Locate and identify every blood parasite.
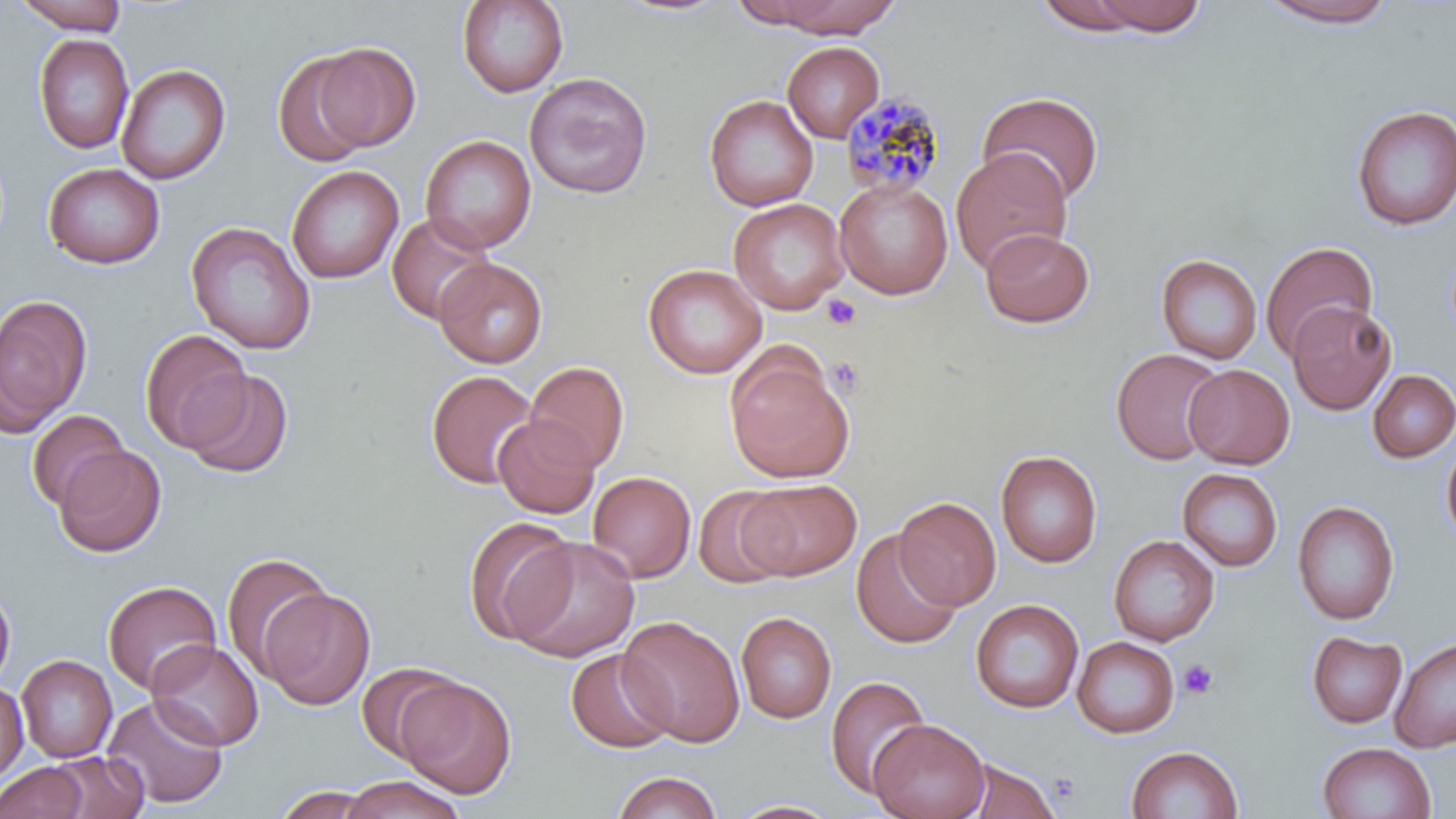
Approximate bounding boxes as named x1/y1/x2/y2 corners in pixels.
Plasmodium malariae-infected red blood cells: (x1=840, y1=90, x2=946, y2=198).
No Plasmodium falciparum, Plasmodium ovale, Plasmodium vivax, Babesia divergens, or Trypanosoma brucei observed.

Summary:
  - Platelet locations: (x1=823, y1=294, x2=861, y2=330), (x1=828, y1=356, x2=863, y2=396), (x1=1178, y1=659, x2=1219, y2=700)
  - Uninfected red blood cell locations: (x1=11, y1=0, x2=129, y2=34), (x1=456, y1=0, x2=569, y2=98), (x1=608, y1=0, x2=736, y2=18), (x1=728, y1=0, x2=834, y2=29), (x1=772, y1=0, x2=900, y2=38), (x1=1090, y1=0, x2=1208, y2=36), (x1=1256, y1=0, x2=1401, y2=28), (x1=1034, y1=1, x2=1147, y2=35), (x1=33, y1=33, x2=133, y2=155), (x1=782, y1=41, x2=884, y2=143), (x1=313, y1=43, x2=420, y2=152), (x1=272, y1=50, x2=376, y2=168), (x1=116, y1=63, x2=230, y2=184), (x1=524, y1=72, x2=653, y2=199), (x1=976, y1=91, x2=1104, y2=206), (x1=704, y1=94, x2=817, y2=211), (x1=1351, y1=104, x2=1456, y2=231), (x1=420, y1=134, x2=536, y2=253), (x1=951, y1=148, x2=1073, y2=275), (x1=43, y1=162, x2=164, y2=269), (x1=286, y1=165, x2=404, y2=284), (x1=834, y1=177, x2=953, y2=300), (x1=729, y1=198, x2=849, y2=315), (x1=386, y1=212, x2=495, y2=325), (x1=185, y1=221, x2=316, y2=355), (x1=980, y1=227, x2=1094, y2=328), (x1=1260, y1=241, x2=1378, y2=361), (x1=1155, y1=254, x2=1262, y2=364), (x1=434, y1=257, x2=547, y2=368), (x1=643, y1=263, x2=768, y2=379), (x1=0, y1=293, x2=92, y2=435), (x1=1287, y1=300, x2=1396, y2=415), (x1=138, y1=329, x2=252, y2=451), (x1=1110, y1=347, x2=1226, y2=466), (x1=726, y1=353, x2=854, y2=484), (x1=525, y1=361, x2=630, y2=472), (x1=1184, y1=364, x2=1294, y2=469), (x1=180, y1=369, x2=294, y2=479), (x1=1367, y1=369, x2=1456, y2=463), (x1=426, y1=370, x2=539, y2=489), (x1=26, y1=409, x2=130, y2=512), (x1=493, y1=414, x2=600, y2=518), (x1=1441, y1=436, x2=1456, y2=549), (x1=55, y1=445, x2=166, y2=557), (x1=995, y1=449, x2=1103, y2=568), (x1=1177, y1=468, x2=1284, y2=571), (x1=587, y1=471, x2=696, y2=583), (x1=739, y1=480, x2=862, y2=580), (x1=692, y1=486, x2=794, y2=589), (x1=893, y1=497, x2=1001, y2=610), (x1=1292, y1=500, x2=1400, y2=625), (x1=463, y1=516, x2=579, y2=646), (x1=851, y1=530, x2=962, y2=650), (x1=1108, y1=535, x2=1220, y2=646), (x1=506, y1=536, x2=641, y2=662), (x1=220, y1=551, x2=334, y2=679), (x1=103, y1=580, x2=222, y2=695), (x1=0, y1=586, x2=16, y2=692), (x1=259, y1=587, x2=376, y2=710), (x1=970, y1=599, x2=1083, y2=713), (x1=736, y1=612, x2=837, y2=724), (x1=618, y1=616, x2=744, y2=746), (x1=1306, y1=631, x2=1407, y2=728), (x1=1072, y1=636, x2=1179, y2=739), (x1=1390, y1=636, x2=1456, y2=753), (x1=147, y1=641, x2=264, y2=751), (x1=565, y1=648, x2=677, y2=754), (x1=16, y1=655, x2=117, y2=762), (x1=357, y1=663, x2=462, y2=762), (x1=824, y1=675, x2=931, y2=799), (x1=395, y1=676, x2=517, y2=800), (x1=0, y1=682, x2=28, y2=783), (x1=102, y1=695, x2=229, y2=809), (x1=869, y1=718, x2=989, y2=819), (x1=1317, y1=742, x2=1436, y2=819), (x1=1126, y1=744, x2=1244, y2=819), (x1=44, y1=750, x2=148, y2=819), (x1=955, y1=758, x2=1062, y2=819), (x1=1, y1=761, x2=89, y2=819), (x1=613, y1=771, x2=722, y2=819), (x1=340, y1=775, x2=465, y2=819), (x1=270, y1=786, x2=383, y2=818), (x1=725, y1=798, x2=845, y2=818)
  - Slide-level diagnosis: Plasmodium malariae
  - Magnification: 1000x
  - Stain: May-Grünwald-Giemsa
  - Image size: 1456×819 pixels
  - Field of view: one of a larger specimen
  - Modality: optical microscopy
  - Preparation: thin blood smear